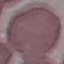
result = no malaria parasites detected
preparation = thin smear
image type = cell patch, automatically extracted from a larger field of view and resized to 64 × 64 pixels
stain = Giemsa
capture = smartphone through the microscope eyepiece